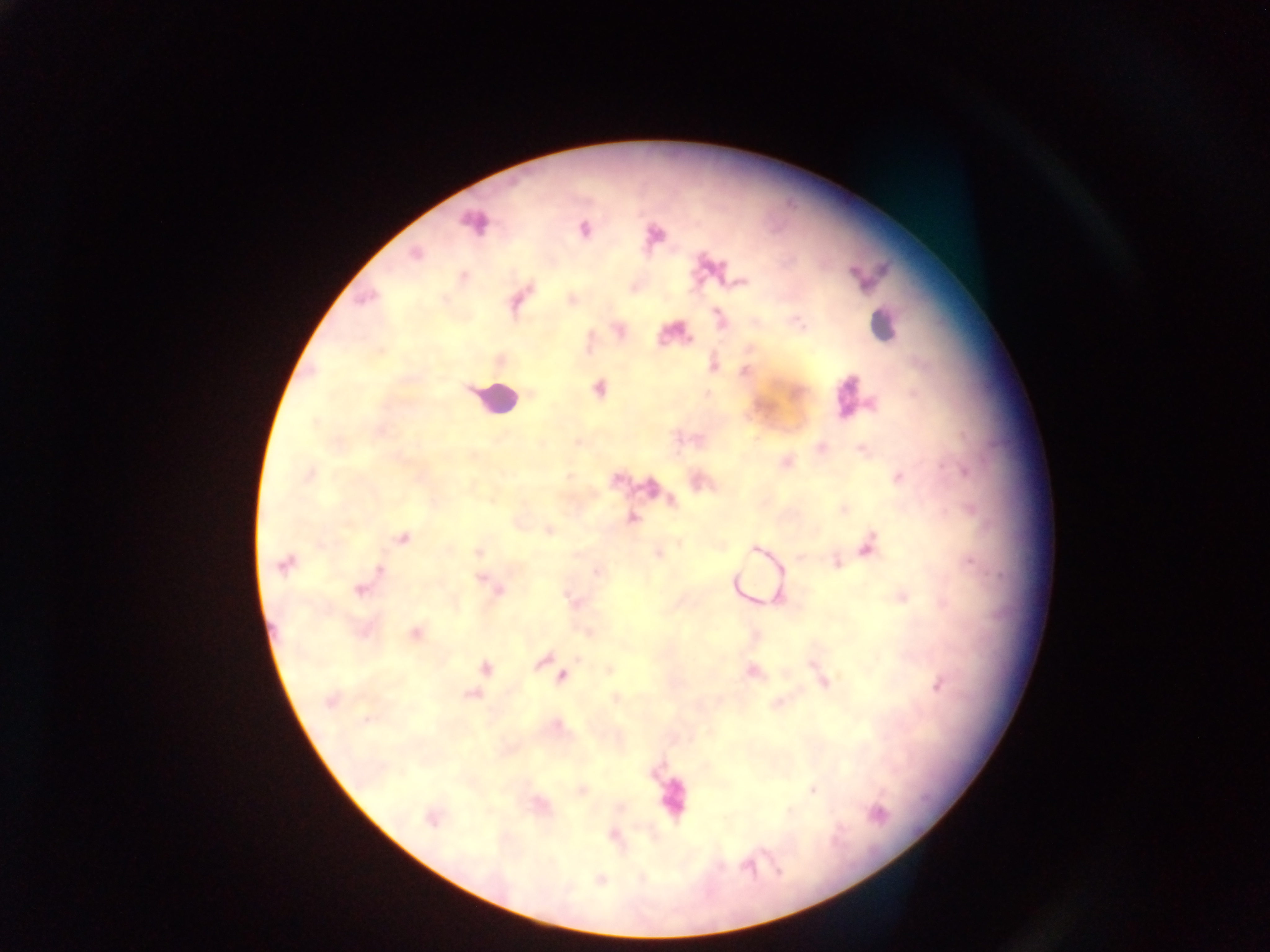

Approximate centers as [x, y] in pixels.
Summary:
  - Leukocyte locations: [883, 326], [496, 399]
  - Malaria parasite locations: [473, 222], [584, 230], [655, 233], [415, 254], [464, 277], [741, 283], [365, 299], [573, 299], [720, 317], [798, 322], [714, 364], [746, 372], [599, 389], [315, 423], [309, 475], [569, 477], [898, 478], [844, 509], [632, 517], [549, 530], [403, 539], [868, 544], [755, 548], [478, 552], [657, 555], [284, 564], [837, 564], [380, 570], [598, 572], [481, 578], [360, 590], [498, 590], [903, 596], [573, 601], [416, 634], [543, 660], [486, 668], [752, 671], [561, 677], [822, 680], [938, 685], [471, 695], [615, 698], [329, 701], [813, 791], [877, 813], [432, 819], [613, 835], [747, 866]
  - Field of view: single
  - Capture: mobile-phone photograph through a microscope
  - Preparation: thick blood smear
  - Country: Ghana
  - Image size: 1270×952 pixels